Report the malaria status.
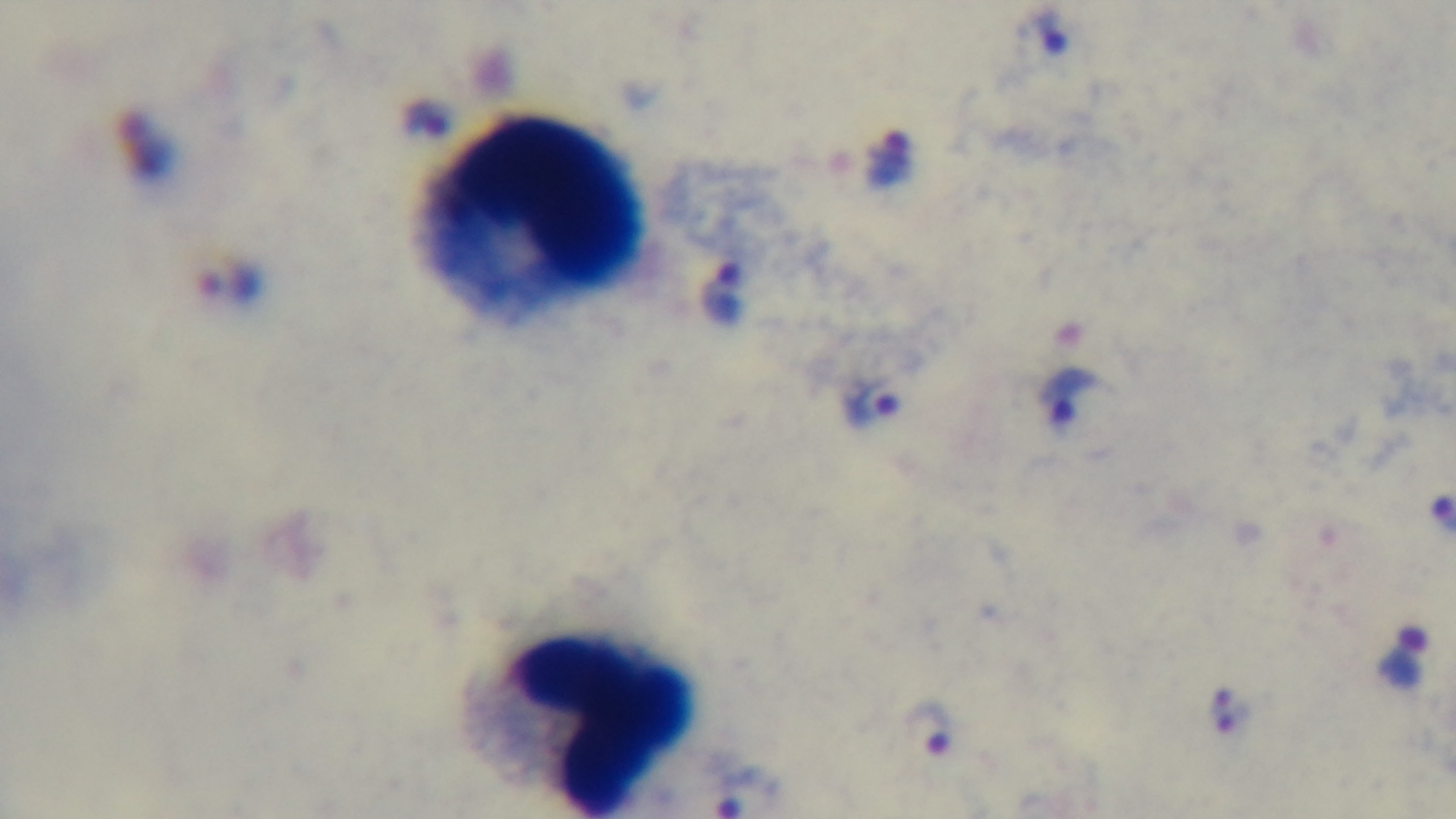

It is infected.

preparation = thick
stain = Giemsa
modality = light microscopy
objective = 100x oil immersion
capture = mounted 4K digital camera
field of view = single